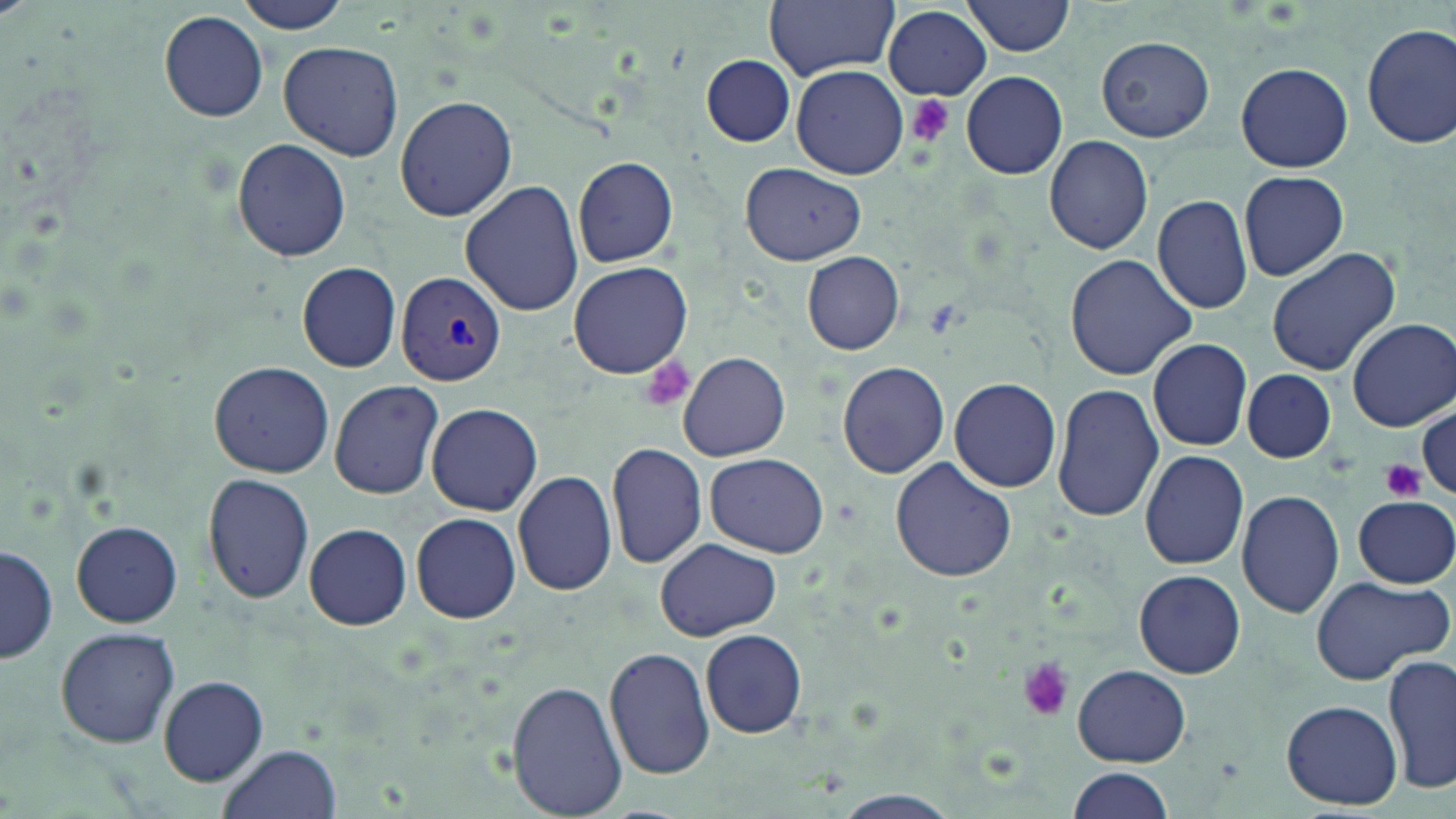
slide_level_diagnosis: Plasmodium vivax
platelet_locations: 'approximate bounding boxes as [x1, y1, x2, y2] in pixels: [903, 93, 958, 147], [640, 354, 696, 413], [1379, 458, 1426, 503], [1015, 656, 1074, 721]'
magnification: 1000x
preparation: thin blood film
modality: light microscopy
plasmodium_vivax_infected_red_blood_cell_locations: 'approximate bounding boxes as [x1, y1, x2, y2] in pixels: [396, 269, 507, 388]'
stain: May-Grünwald-Giemsa
uninfected_red_blood_cell_locations: 'approximate bounding boxes as [x1, y1, x2, y2] in pixels: [237, 0, 352, 33], [763, 0, 899, 79], [963, 0, 1076, 56], [883, 6, 992, 101], [158, 10, 269, 123], [1361, 24, 1456, 151], [1097, 36, 1213, 141], [277, 41, 404, 161], [702, 55, 795, 147], [1236, 63, 1353, 172], [791, 65, 909, 179], [959, 70, 1068, 180], [395, 95, 517, 222], [1043, 134, 1154, 254], [231, 137, 352, 262], [572, 156, 678, 268], [740, 164, 866, 265], [1239, 171, 1349, 281], [458, 182, 583, 319], [1151, 194, 1255, 315], [1265, 247, 1401, 375], [802, 252, 905, 354], [1064, 254, 1199, 381], [298, 261, 402, 373], [567, 261, 693, 379], [1348, 319, 1455, 430], [1148, 338, 1253, 452], [677, 353, 791, 461], [207, 359, 333, 478], [837, 361, 951, 478], [1243, 369, 1335, 462], [949, 376, 1062, 493], [329, 380, 444, 499], [1052, 382, 1162, 522], [427, 403, 543, 516], [1415, 404, 1455, 502], [605, 440, 708, 570], [1138, 449, 1249, 571], [706, 453, 828, 559], [890, 458, 1019, 584], [513, 469, 617, 597], [202, 471, 317, 605], [1236, 490, 1345, 617], [1353, 495, 1456, 587], [410, 511, 521, 624], [72, 521, 182, 627], [304, 524, 411, 631], [656, 537, 781, 640], [1, 543, 57, 666], [1133, 569, 1245, 678], [1310, 577, 1450, 688], [56, 627, 182, 748], [700, 629, 806, 738], [605, 645, 718, 780], [1384, 655, 1455, 797], [1071, 663, 1191, 767], [159, 676, 267, 785], [506, 679, 628, 818], [1282, 699, 1404, 809], [219, 743, 342, 819], [1065, 768, 1174, 819]'
field_of_view: one of a larger specimen
image_size: 1456×819 pixels